Classify this cell by malaria status.
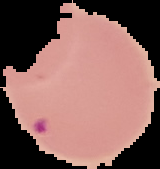
Parasitized.

Image is 160×169 pixels. The area outside the segmented cell region is set to black. From a thin blood smear.